Identify the blood parasite species.
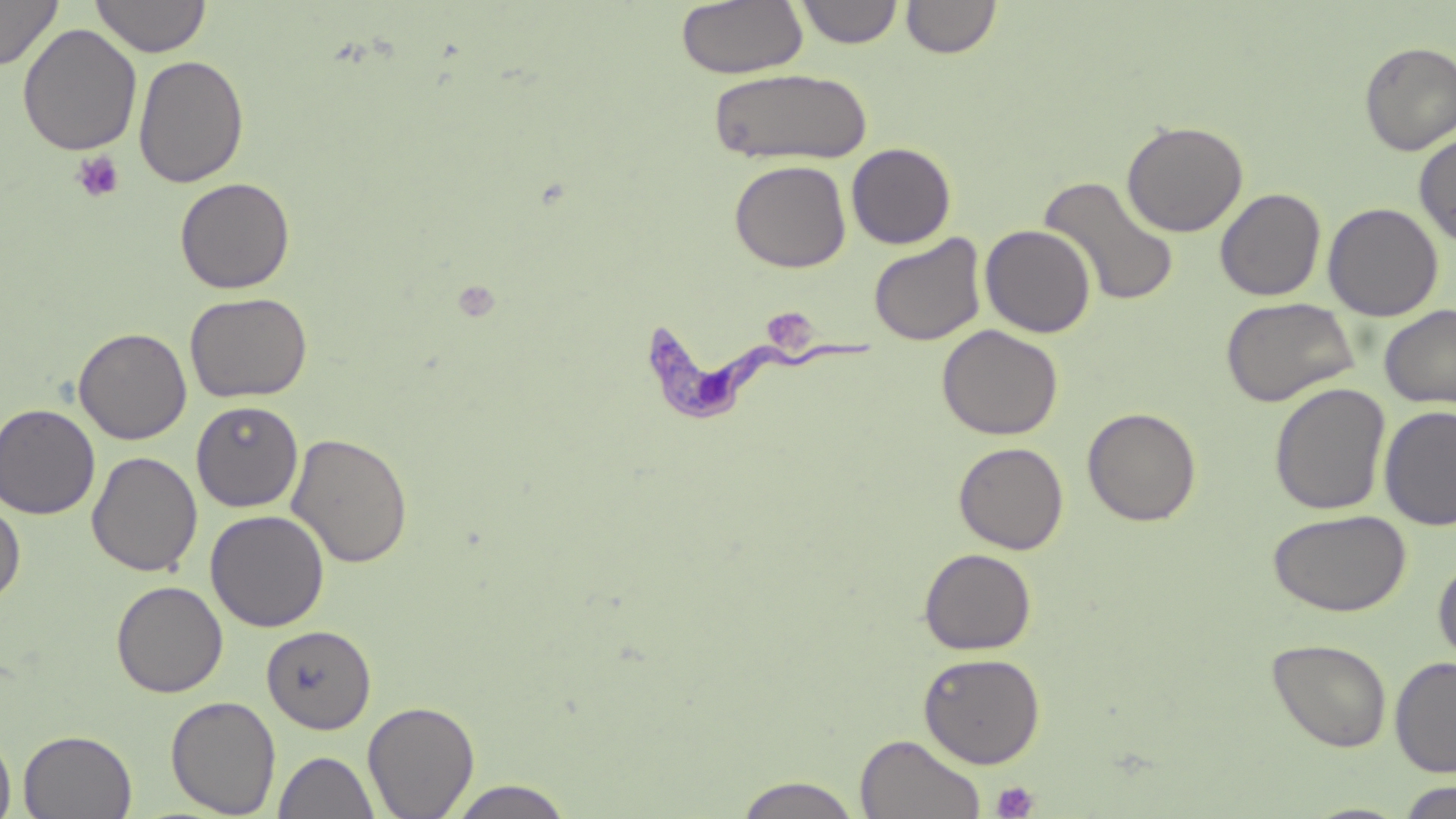
Trypanosoma brucei.

Approximate bounding boxes as (x1,y1)-(x2,y2) corner pairs in pixels. Uninfected red blood cell locations: (0,0)-(62,70), (90,0)-(211,57), (795,0)-(904,48), (675,1)-(808,79), (902,1)-(1002,59), (17,24)-(142,156), (1358,41)-(1456,156), (133,54)-(249,188), (708,68)-(872,165), (1121,119)-(1248,237), (1414,130)-(1456,248), (847,142)-(956,249), (729,160)-(851,272), (175,176)-(295,294), (1038,176)-(1180,307), (1215,187)-(1326,301), (1323,202)-(1443,321), (979,224)-(1096,338), (869,233)-(987,346), (184,292)-(313,403), (1220,297)-(1358,406), (1379,305)-(1456,408), (937,324)-(1063,440), (73,327)-(192,445), (1269,382)-(1391,515), (191,400)-(304,512), (0,403)-(100,519), (1378,404)-(1456,531), (1082,406)-(1201,526), (287,432)-(413,569), (954,441)-(1069,554), (87,451)-(203,577), (0,497)-(26,606), (205,509)-(330,632), (1267,509)-(1411,617), (919,548)-(1036,655), (1433,558)-(1456,667), (112,580)-(228,697), (261,625)-(377,734), (1268,637)-(1392,753), (918,652)-(1045,768), (1390,655)-(1456,777), (166,695)-(281,817), (363,699)-(480,818), (19,729)-(137,818), (0,730)-(16,819), (855,734)-(987,819), (273,750)-(380,819), (733,775)-(864,819), (445,780)-(576,819), (1395,781)-(1456,818). Trypanosoma brucei locations: (647,311)-(874,425). Platelet locations: (71,151)-(124,203), (756,306)-(820,352), (992,781)-(1039,819). Image is 1456×819 pixels. Single field of view. May-Grünwald-Giemsa stain. Light microscopy. Thin blood smear. Captured at 1000x magnification.